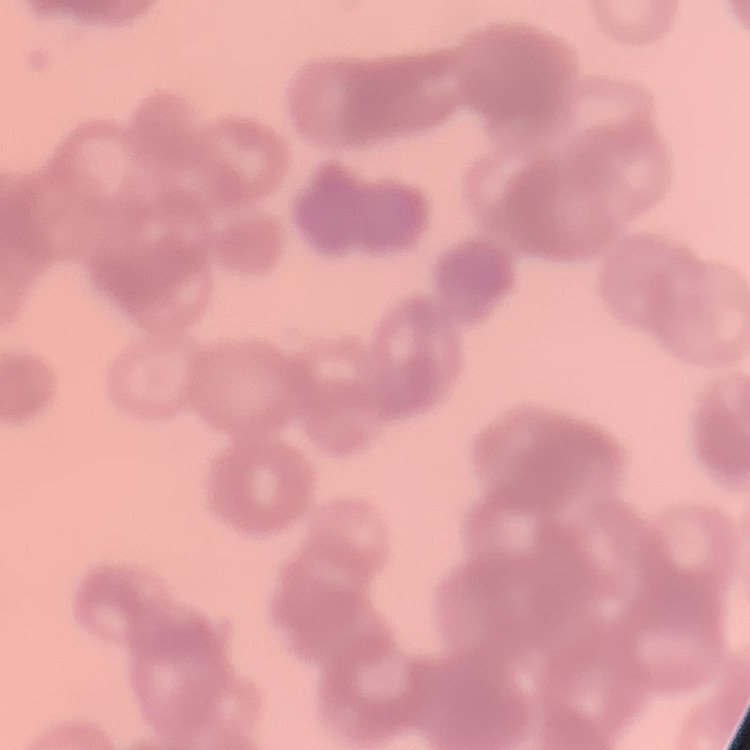

Summary:
  - Erythrocyte morphology: rouleaux formation
  - Image type: square crop of a larger photomicrograph
  - Stain: Field's or Giemsa
  - Preparation: thin blood smear